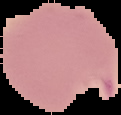
Summary:
  - Result: malaria parasites identified
  - Preparation: thin blood smear
  - Image type: cell region segmented out of the field of view; surrounding area masked to black
  - Image size: 121×115 pixels